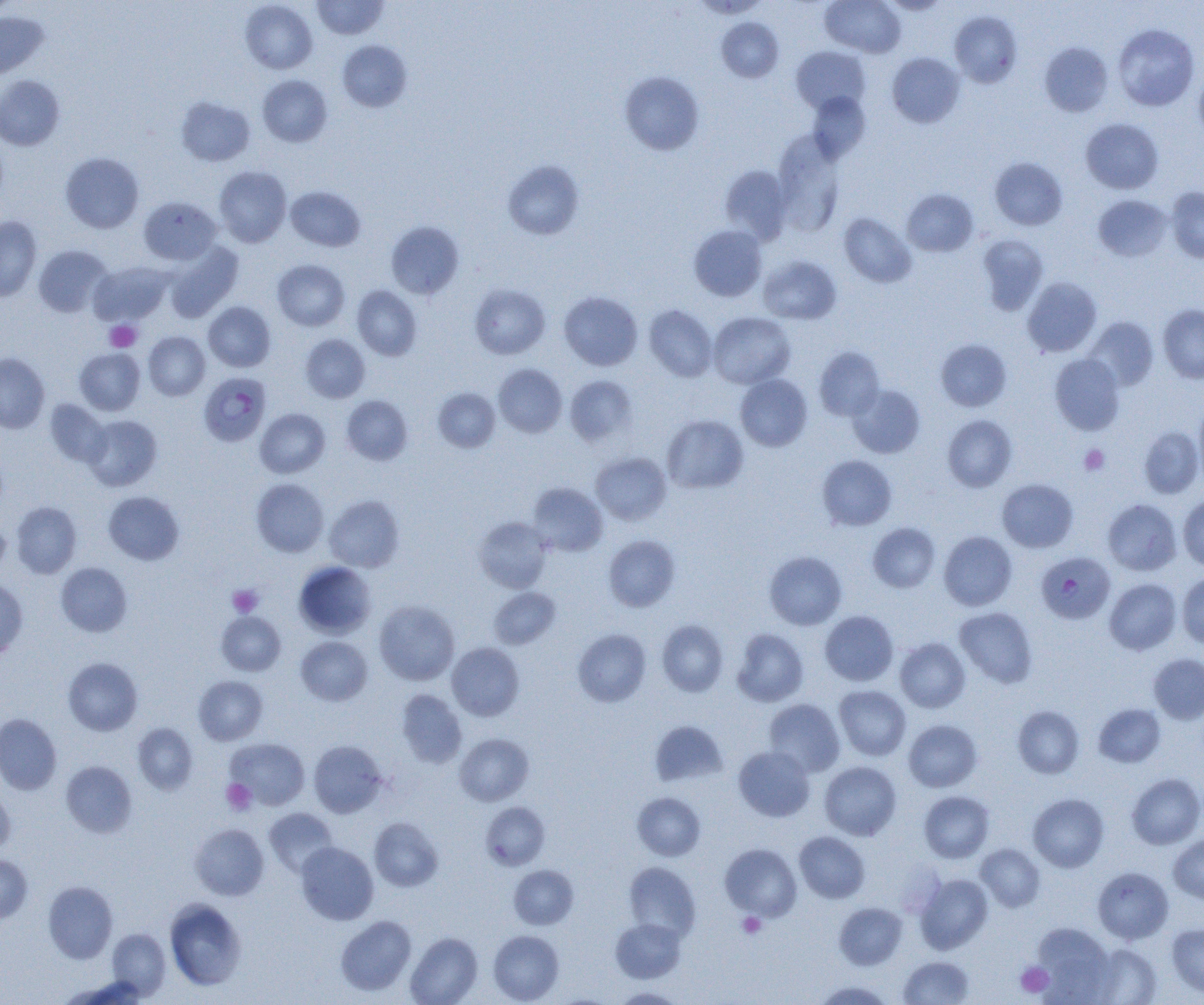 Approximate bounding boxes as (x1,y1)-(x2,y2) corner pairs in pixels. Uninfected red blood cell locations (subset): (312,0)-(388,39), (820,0)-(905,58), (880,0)-(950,14), (0,1)-(18,20), (240,1)-(317,74), (950,10)-(1022,88), (0,11)-(49,79), (717,17)-(783,83), (1112,24)-(1199,111), (337,40)-(412,112), (1040,42)-(1113,117), (791,46)-(870,114), (887,52)-(965,128), (1194,67)-(1204,145), (619,71)-(704,155), (0,75)-(64,150), (257,75)-(332,147), (806,92)-(870,162), (175,96)-(255,166), (1080,118)-(1163,194), (772,131)-(846,236), (60,152)-(144,233), (990,157)-(1067,230), (503,160)-(584,240), (720,165)-(792,245), (214,166)-(291,248), (286,185)-(366,251), (1166,187)-(1204,263), (902,188)-(978,256), (1093,195)-(1173,262), (138,196)-(220,265), (838,212)-(916,288), (0,216)-(41,301), (386,221)-(464,299), (689,225)-(767,301), (977,234)-(1049,315), (162,241)-(244,322), (33,245)-(112,317), (758,255)-(841,325), (272,259)-(350,331), (89,261)-(172,325), (1022,277)-(1102,357), (469,284)-(550,360), (352,286)-(422,360), (559,291)-(642,370), (203,301)-(276,372), (1158,304)-(1204,383), (644,305)-(717,382), (708,312)-(795,388), (1083,317)-(1158,392), (144,331)-(210,400), (300,334)-(370,403), (935,339)-(1012,411), (814,347)-(884,420), (74,348)-(145,415), (0,353)-(50,433), (1050,353)-(1124,435), (493,364)-(567,437), (735,374)-(812,451), (565,375)-(637,447), (847,384)-(926,458), (433,388)-(500,452), (342,395)-(413,465), (45,400)-(110,467), (1193,402)-(1204,485), (255,408)-(330,478), (662,414)-(748,493), (83,415)-(162,491), (942,415)-(1017,491), (1138,426)-(1203,499), (591,452)-(670,524), (817,455)-(897,531), (251,478)-(329,556), (997,478)-(1078,552), (528,482)-(607,556), (103,491)-(184,565), (324,495)-(404,572), (1178,496)-(1204,570), (1103,498)-(1181,576), (11,501)-(81,578), (474,516)-(553,593), (867,522)-(940,593), (0,523)-(10,574), (938,531)-(1017,610), (604,535)-(680,611), (764,551)-(847,630), (294,561)-(376,639), (56,562)-(132,637), (1177,573)-(1204,648), (1104,578)-(1181,655), (0,579)-(28,660), (489,587)-(560,649), (374,600)-(459,685), (954,607)-(1038,688), (820,610)-(898,686), (216,612)-(285,675), (657,619)-(729,696), (573,628)-(651,707), (732,629)-(808,706), (296,636)-(372,706), (895,638)-(970,713), (447,643)-(524,721), (1148,653)-(1204,724), (63,657)-(142,735), (193,675)-(267,745), (834,685)-(911,760), (397,689)-(467,768), (763,699)-(845,777), (1093,703)-(1165,767), (1013,706)-(1084,779), (0,713)-(61,795), (903,719)-(982,792), (649,721)-(728,787), (133,723)-(198,794), (455,733)-(534,806), (225,738)-(310,810), (309,740)-(387,817), (733,745)-(815,822), (61,761)-(137,838), (819,761)-(902,840), (1127,773)-(1204,849), (0,787)-(15,854), (919,790)-(994,863), (632,791)-(706,861), (1028,793)-(1109,872), (481,802)-(550,869), (264,807)-(338,877), (369,817)-(443,892), (190,823)-(269,900), (794,831)-(870,903), (1169,831)-(1204,903), (296,842)-(379,925), (720,843)-(802,921), (975,844)-(1045,912), (0,854)-(33,923), (623,862)-(700,941), (508,865)-(579,929), (1093,866)-(1174,944), (915,873)-(993,953), (43,881)-(117,963), (165,898)-(246,990), (834,902)-(907,970), (335,916)-(416,996), (610,918)-(686,983), (1031,922)-(1116,1004), (1167,923)-(1204,998), (107,928)-(171,998), (488,930)-(564,1004), (406,932)-(482,1005), (1087,943)-(1162,1005), (899,956)-(974,1004), (59,975)-(150,1005), (812,980)-(895,1005), (611,987)-(685,1004). Platelet locations: (105,320)-(141,352), (1079,444)-(1110,475), (228,584)-(263,617), (221,779)-(256,815), (738,912)-(766,938), (1015,961)-(1054,997). Plasmodium falciparum-infected red blood cell locations (subset): (1036,552)-(1115,624). Slide-level diagnosis: Plasmodium falciparum. Image is 1204×1005 pixels. One field of a larger specimen. Captured at 1000x magnification. Optical microscopy. Thin blood smear.